Classify this cell by malaria status.
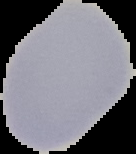
Uninfected.

Image is 136×154 pixels. The area outside the segmented cell region is set to black. From a thin blood smear.